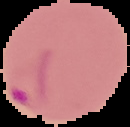

result = malaria parasites detected
preparation = thin blood smear
image type = cell region segmented out of the field of view; surrounding area masked to black
image size = 130×127 pixels